Identify the preparation type.
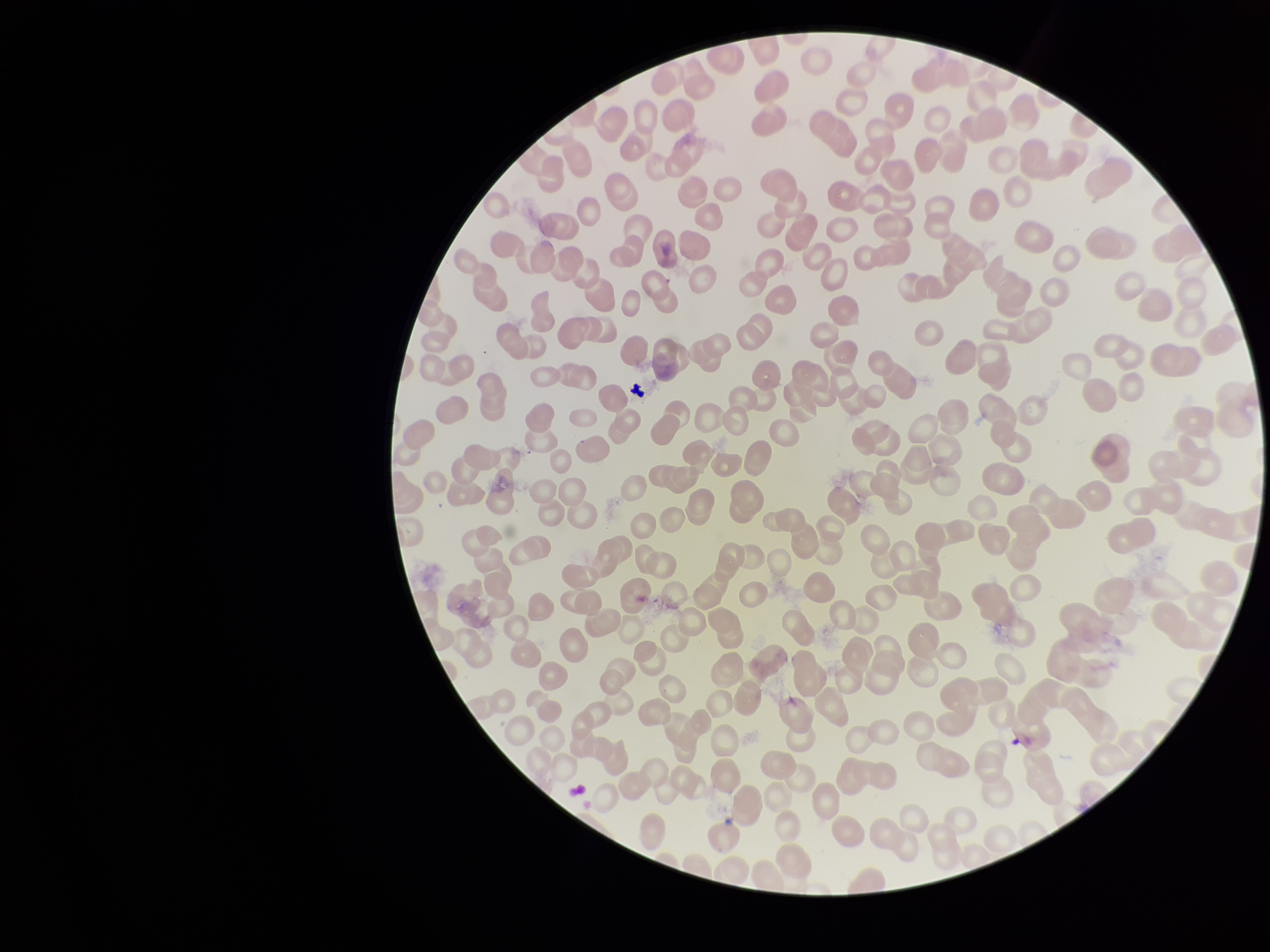

A thin smear.

Patient malaria status: negative. Giemsa stain. Single field of view. Image is 1270×952 pixels. Parasitized red blood cells: none identified. Smartphone photograph taken through the eyepiece of a microscope. Red blood cell count: 247. Parasitized red blood cell count: 0.